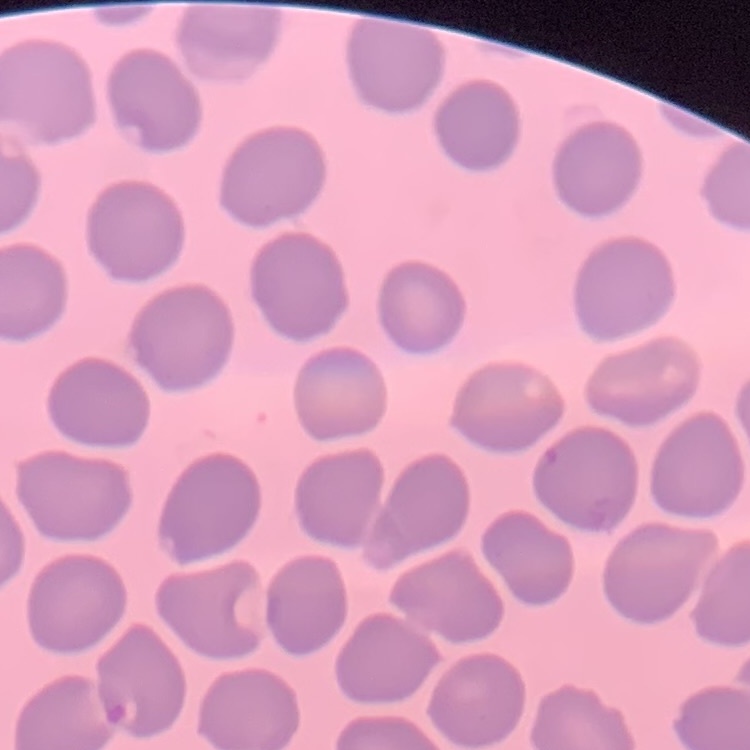

The erythrocytes show no rouleaux formation. One tile cut from a larger photomicrograph. Field's or Giemsa stain. Thin blood film.